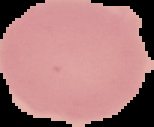
{
  "preparation": "thin blood smear",
  "image_type": "segmented cell region on a black background",
  "malaria_status": "uninfected",
  "image_size": "154×127 pixels"
}